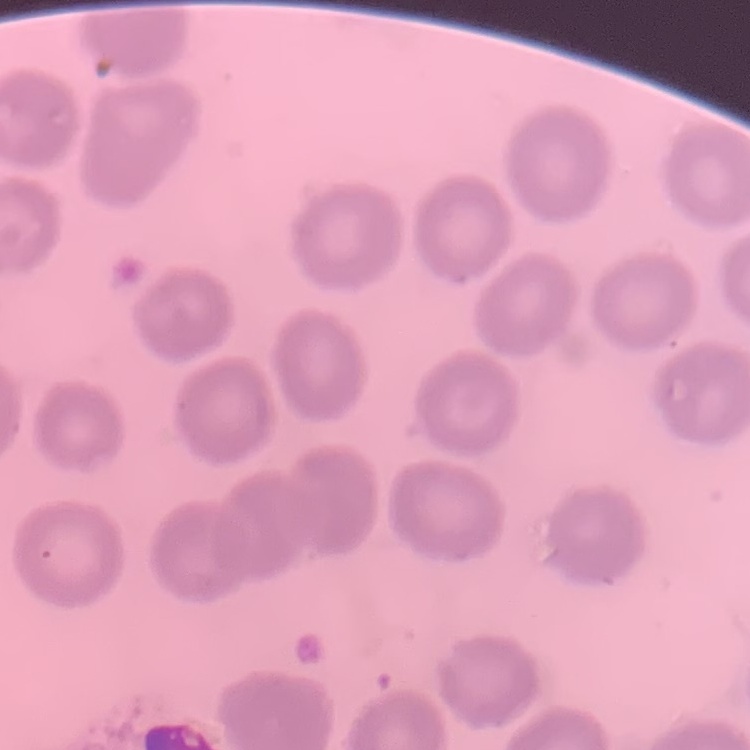
The red blood cells show no rouleaux formation. Stained with either Field's or Giemsa. Square crop of a larger photomicrograph. Thin peripheral smear.